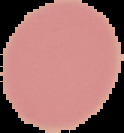
Summary:
  - Result: no Plasmodium parasites seen
  - Preparation: thin blood film
  - Image size: 124×133 pixels
  - Image type: segmented cell region on a black background